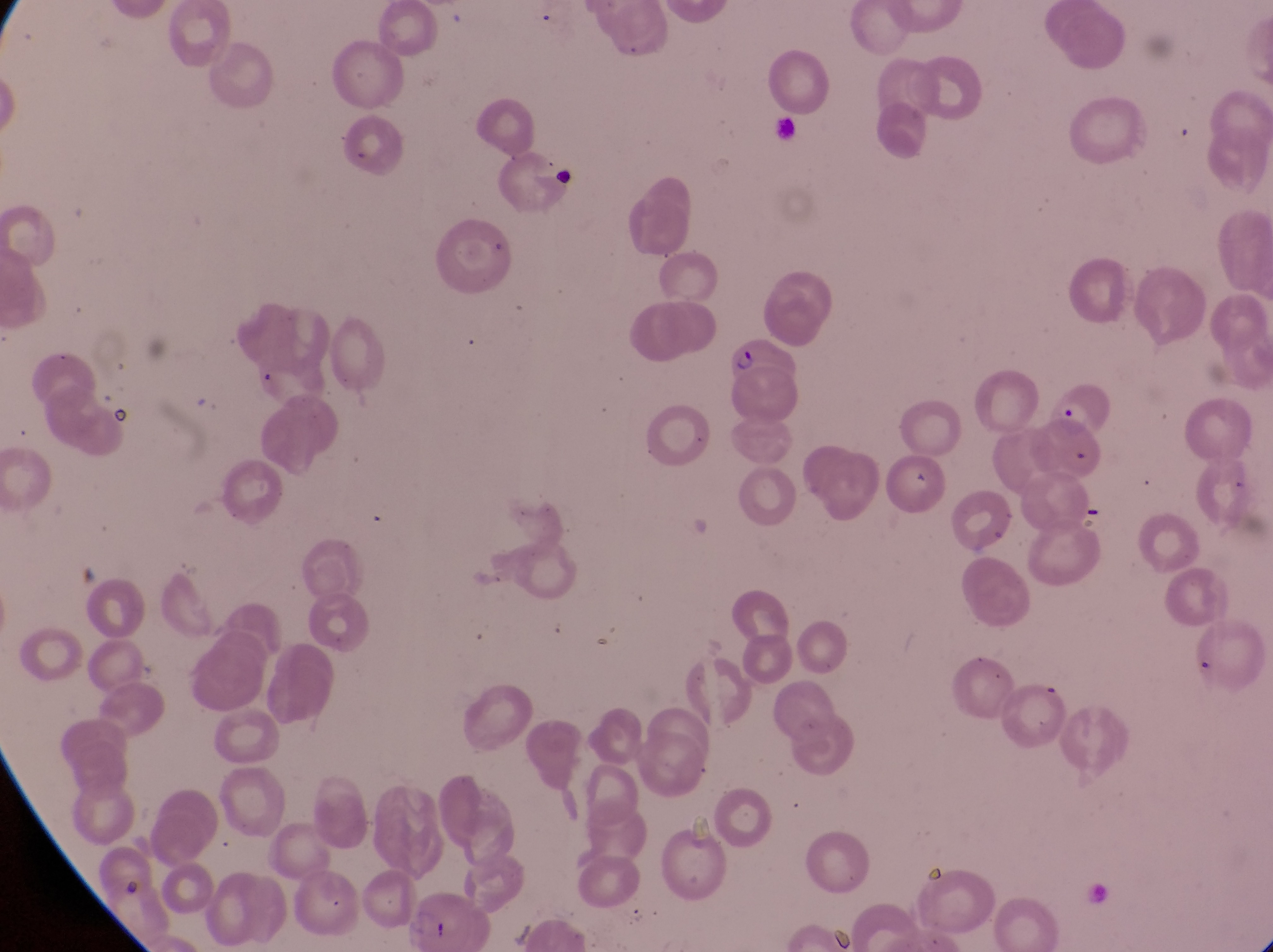

Approximate bounding boxes as [left, top, right, bottom] in pixels. Parasitised red blood cell locations: [726, 330, 800, 420], [1044, 377, 1118, 451]. Artifact (platelet-like body, stain precipitate, or debris) locations: [1076, 499, 1108, 526]. Leukocyte locations: [547, 162, 577, 195]. At a magnification of 1000x. Collected in Uganda. Thin blood film. Single field of view. Image is 1273×952 pixels. Captured by a smartphone held over the eyepiece of an Olympus CX-23 microscope.